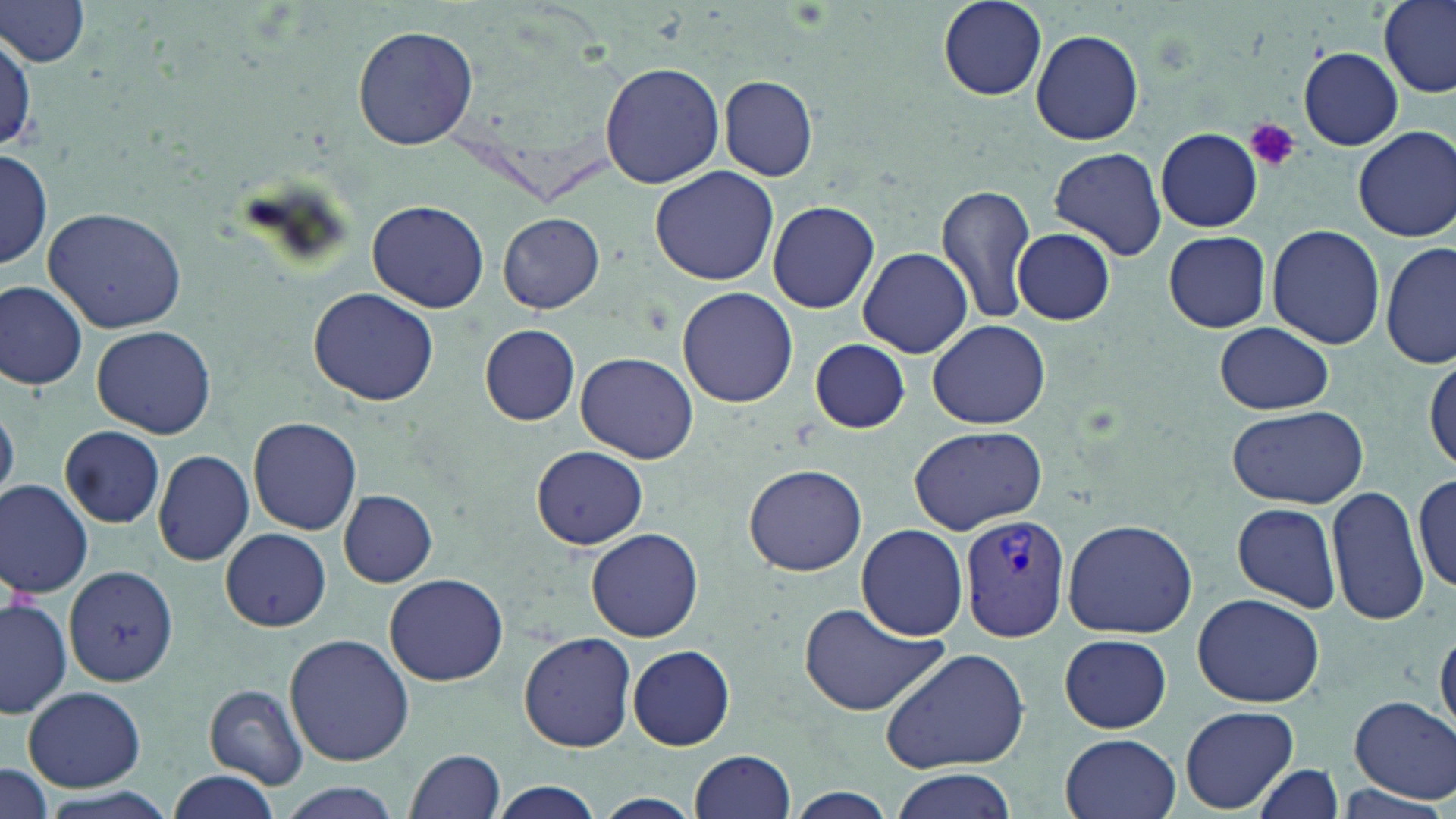
Summary:
  - Coordinate format: approximate bounding boxes as named x1/y1/x2/y2 corners in pixels
  - Plasmodium vivax-infected red blood cell locations: (x1=958, y1=512, x2=1071, y2=644)
  - Platelet locations: (x1=1246, y1=118, x2=1298, y2=171)
  - Uninfected red blood cell locations: (x1=937, y1=0, x2=1046, y2=99), (x1=1377, y1=0, x2=1456, y2=100), (x1=0, y1=1, x2=94, y2=67), (x1=353, y1=26, x2=478, y2=149), (x1=1030, y1=29, x2=1144, y2=146), (x1=0, y1=35, x2=35, y2=152), (x1=1299, y1=47, x2=1403, y2=150), (x1=600, y1=61, x2=725, y2=189), (x1=718, y1=74, x2=818, y2=182), (x1=1353, y1=127, x2=1456, y2=240), (x1=1156, y1=129, x2=1262, y2=232), (x1=1049, y1=146, x2=1167, y2=260), (x1=0, y1=147, x2=50, y2=273), (x1=649, y1=166, x2=778, y2=285), (x1=937, y1=182, x2=1038, y2=328), (x1=368, y1=200, x2=489, y2=311), (x1=768, y1=200, x2=880, y2=313), (x1=42, y1=206, x2=189, y2=334), (x1=498, y1=213, x2=605, y2=312), (x1=1266, y1=223, x2=1385, y2=351), (x1=1012, y1=227, x2=1114, y2=324), (x1=1163, y1=231, x2=1270, y2=332), (x1=1381, y1=242, x2=1455, y2=369), (x1=856, y1=246, x2=975, y2=359), (x1=0, y1=282, x2=87, y2=389), (x1=677, y1=287, x2=799, y2=407), (x1=309, y1=289, x2=437, y2=404), (x1=925, y1=319, x2=1051, y2=428), (x1=1215, y1=321, x2=1333, y2=416), (x1=480, y1=325, x2=579, y2=424), (x1=91, y1=326, x2=216, y2=437), (x1=810, y1=339, x2=910, y2=432), (x1=575, y1=353, x2=697, y2=464), (x1=1426, y1=355, x2=1456, y2=474), (x1=1228, y1=404, x2=1368, y2=509), (x1=248, y1=418, x2=362, y2=536), (x1=909, y1=424, x2=1047, y2=534), (x1=60, y1=425, x2=166, y2=529), (x1=532, y1=446, x2=649, y2=550), (x1=153, y1=449, x2=255, y2=567), (x1=743, y1=463, x2=867, y2=576), (x1=1414, y1=470, x2=1455, y2=596), (x1=1363, y1=473, x2=1456, y2=609), (x1=0, y1=482, x2=94, y2=598), (x1=1327, y1=485, x2=1428, y2=624), (x1=338, y1=490, x2=437, y2=587), (x1=1230, y1=500, x2=1342, y2=613), (x1=1062, y1=518, x2=1197, y2=639), (x1=857, y1=524, x2=970, y2=642), (x1=586, y1=527, x2=704, y2=642), (x1=220, y1=528, x2=330, y2=631), (x1=64, y1=564, x2=178, y2=687), (x1=384, y1=573, x2=509, y2=685), (x1=1193, y1=592, x2=1324, y2=709), (x1=0, y1=598, x2=72, y2=717), (x1=796, y1=601, x2=950, y2=716), (x1=1434, y1=626, x2=1456, y2=737), (x1=519, y1=632, x2=636, y2=752), (x1=285, y1=634, x2=415, y2=765), (x1=1056, y1=634, x2=1175, y2=733), (x1=628, y1=644, x2=736, y2=750), (x1=880, y1=647, x2=1030, y2=772), (x1=201, y1=684, x2=310, y2=789), (x1=23, y1=686, x2=147, y2=792), (x1=1349, y1=694, x2=1455, y2=802), (x1=1180, y1=705, x2=1299, y2=813), (x1=1061, y1=732, x2=1181, y2=819), (x1=406, y1=750, x2=504, y2=819), (x1=689, y1=750, x2=796, y2=819), (x1=0, y1=762, x2=53, y2=817), (x1=1251, y1=764, x2=1345, y2=819), (x1=889, y1=768, x2=1020, y2=819), (x1=169, y1=770, x2=282, y2=818), (x1=485, y1=780, x2=605, y2=819), (x1=276, y1=784, x2=405, y2=818), (x1=1333, y1=784, x2=1446, y2=819), (x1=783, y1=787, x2=899, y2=819), (x1=597, y1=793, x2=701, y2=816)
  - Slide-level diagnosis: Plasmodium vivax
  - Image size: 1456×819 pixels
  - Stain: May-Grünwald-Giemsa
  - Modality: light microscopy
  - Preparation: thin blood film
  - Field of view: one of a larger specimen
  - Magnification: 1000x